Classify this cell by malaria status.
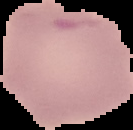

It is uninfected.

preparation: thin blood smear
image_type: cell region segmented out of the field of view; surrounding area masked to black
image_size: 133×130 pixels